Classify this cell by malaria status.
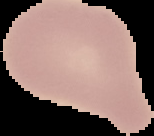

Uninfected.

Image is 154×136 pixels. The area outside the segmented cell region is set to black. From a thin blood smear.